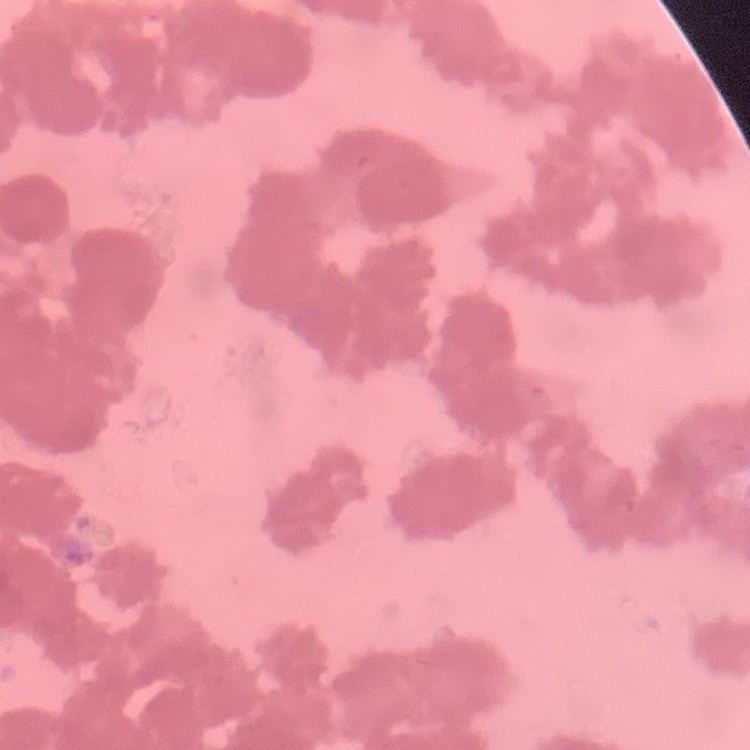

Summary:
  - Red blood cell morphology: rouleaux formation
  - Stain: Field's or Giemsa
  - Preparation: thin blood film
  - Image type: one tile cut from a larger photomicrograph